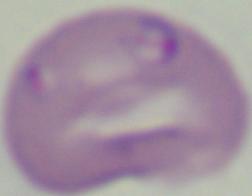

{
  "identification": "Babesia",
  "magnification": "1000x",
  "modality": "photomicrograph"
}